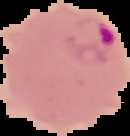
The area outside the segmented cell region is set to black. Result: malaria parasites detected. Image is 130×136 pixels. From a thin blood smear.